Classify this cell by malaria status.
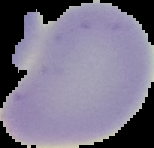
Uninfected.

Summary:
  - Image type: segmented cell region on a black background
  - Preparation: thin blood smear
  - Image size: 154×148 pixels